State which cell type is depicted.
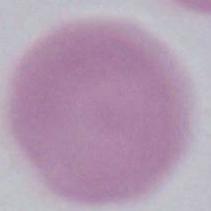

This is an erythrocyte.

Summary:
  - Magnification: 1000x
  - Modality: photomicrograph